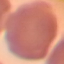

result = no malaria parasites detected
stain = Giemsa
image type = cell patch, automatically extracted from a larger field of view and resized to 64 × 64 pixels
preparation = thin smear
capture = smartphone through the microscope eyepiece